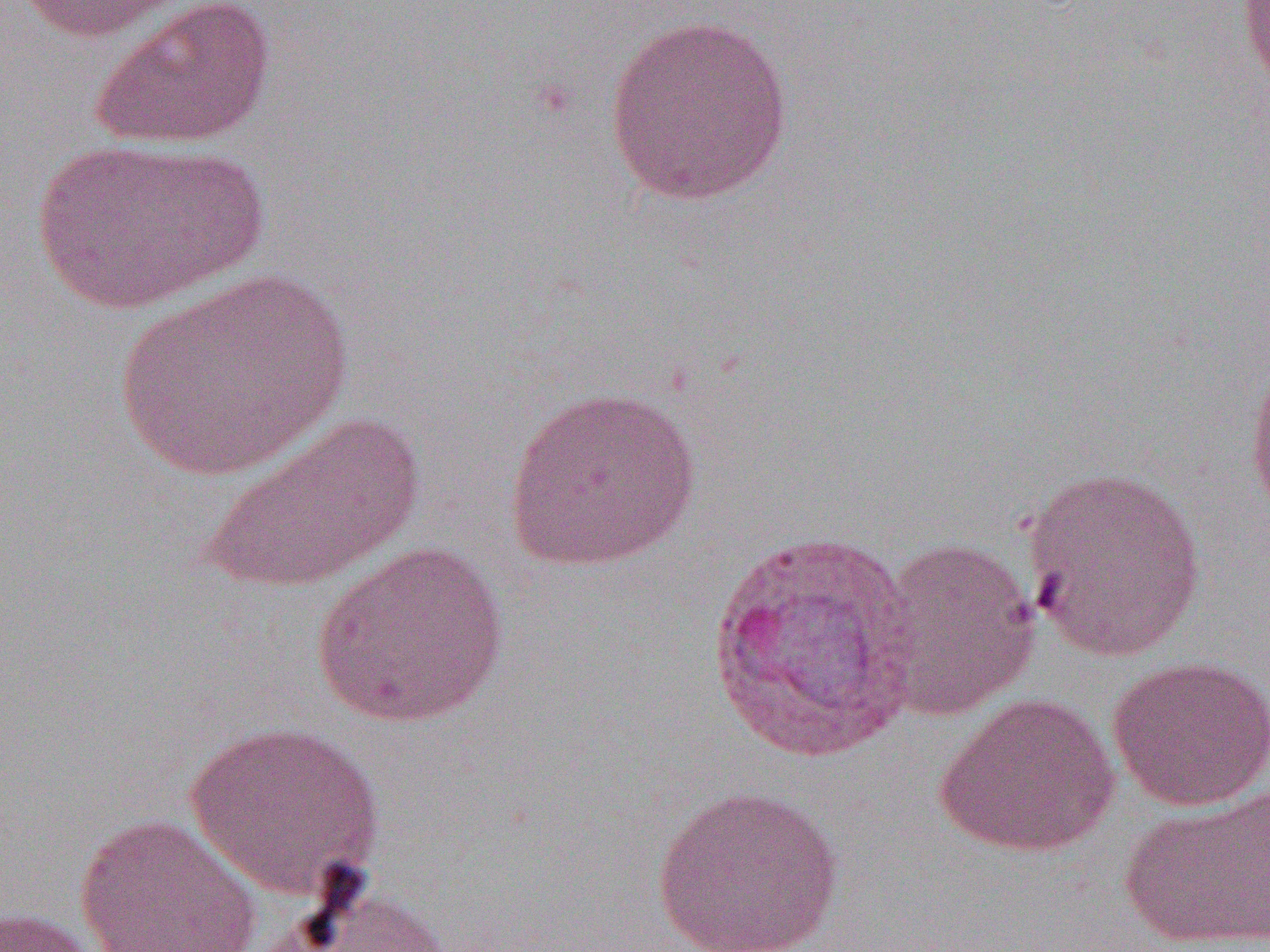
Approximate bounding boxes as (x1, y1, x2, y2) in pixels. Uninfected red blood cell locations: (9, 0, 196, 43), (88, 0, 277, 150), (1237, 0, 1270, 92), (602, 11, 796, 205), (28, 138, 264, 316), (115, 268, 355, 481), (1244, 345, 1270, 528), (504, 383, 702, 571), (197, 410, 427, 595), (1020, 463, 1209, 663), (875, 536, 1041, 719), (311, 541, 510, 730), (1106, 655, 1270, 811), (934, 691, 1120, 858), (184, 719, 385, 900), (650, 784, 847, 952), (1119, 787, 1270, 950), (74, 811, 264, 952), (269, 886, 452, 952), (0, 905, 107, 952). Slide-level diagnosis: Plasmodium vivax. One field of a larger specimen. 1000x magnification. Optical microscopy. Thin blood smear. Image is 1270×952 pixels.